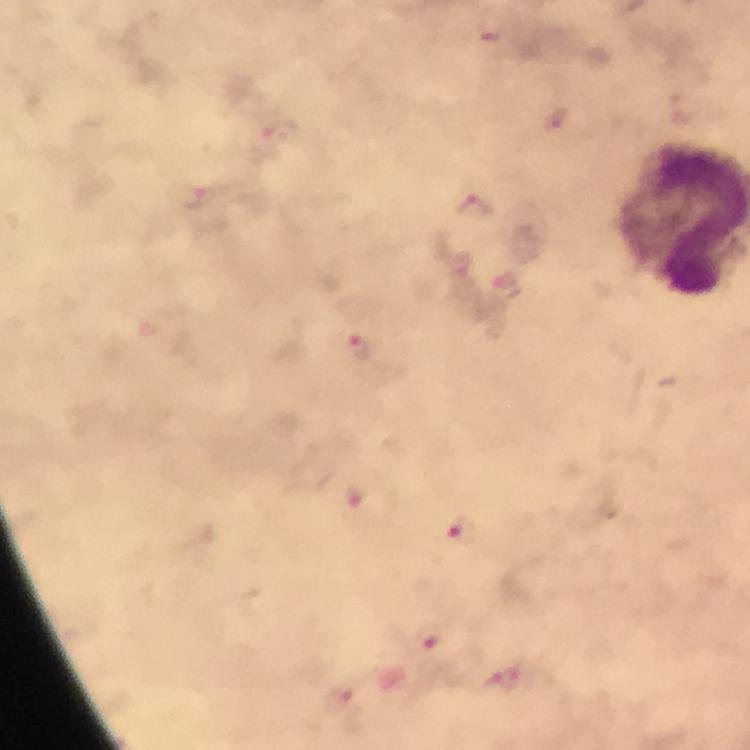
Approximate object centers, in pixels from the top-left corner. Malaria parasite locations: (x=555, y=123), (x=195, y=200), (x=470, y=209), (x=460, y=265), (x=505, y=286), (x=360, y=346), (x=461, y=530), (x=429, y=636). From a diagnostic examination for malaria. Cropped region of a single field of view. Photographed with a smartphone mounted on the microscope. Image is 750×750 pixels. Immersion oil applied. Giemsa stain. At 100x magnification. Thick smear.